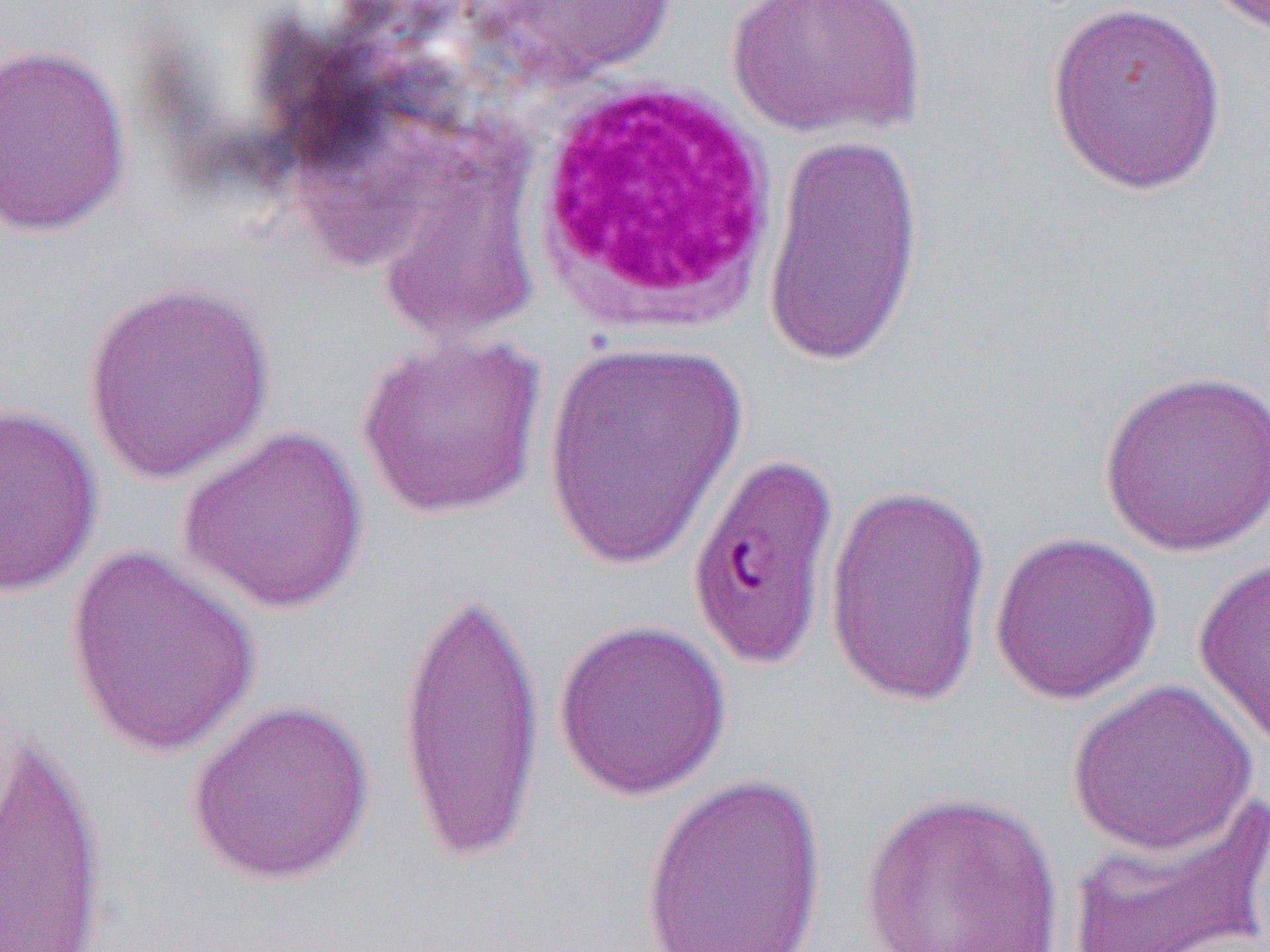

Approximate bounding boxes as named x1/y1/x2/y2 corners in pixels. White blood cell locations: (x1=523, y1=75, x2=783, y2=337). Uninfected red blood cell locations: (x1=477, y1=0, x2=676, y2=86), (x1=725, y1=0, x2=926, y2=140), (x1=1044, y1=1, x2=1229, y2=196), (x1=0, y1=43, x2=133, y2=238), (x1=760, y1=129, x2=925, y2=372), (x1=80, y1=277, x2=276, y2=485), (x1=355, y1=331, x2=548, y2=521), (x1=542, y1=338, x2=749, y2=570), (x1=1098, y1=368, x2=1270, y2=557), (x1=0, y1=401, x2=103, y2=599), (x1=176, y1=423, x2=371, y2=615), (x1=684, y1=446, x2=843, y2=673), (x1=823, y1=481, x2=992, y2=708), (x1=988, y1=530, x2=1163, y2=704), (x1=63, y1=542, x2=264, y2=760), (x1=1193, y1=557, x2=1270, y2=756), (x1=395, y1=579, x2=545, y2=871), (x1=552, y1=618, x2=732, y2=801), (x1=1066, y1=679, x2=1259, y2=857), (x1=185, y1=697, x2=376, y2=887), (x1=1, y1=725, x2=111, y2=952), (x1=640, y1=772, x2=828, y2=952), (x1=857, y1=788, x2=1066, y2=952), (x1=1067, y1=789, x2=1270, y2=952). Slide-level diagnosis: Plasmodium falciparum. 1000x magnification. Light microscopy. One field of a larger specimen. Image is 1270×952 pixels. Thin blood film.